Report the malaria status of this cell.
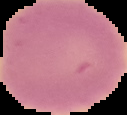
Uninfected.

From a thin blood film. Segmented cell region on a black background. Image is 127×115 pixels.